Report the malaria status of this cell.
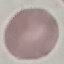
Uninfected.

Acquired by smartphone through the microscope eyepiece. Giemsa-stained preparation. Cell patch, automatically extracted from a larger field of view and resized to 64 × 64 pixels. Thin blood film.